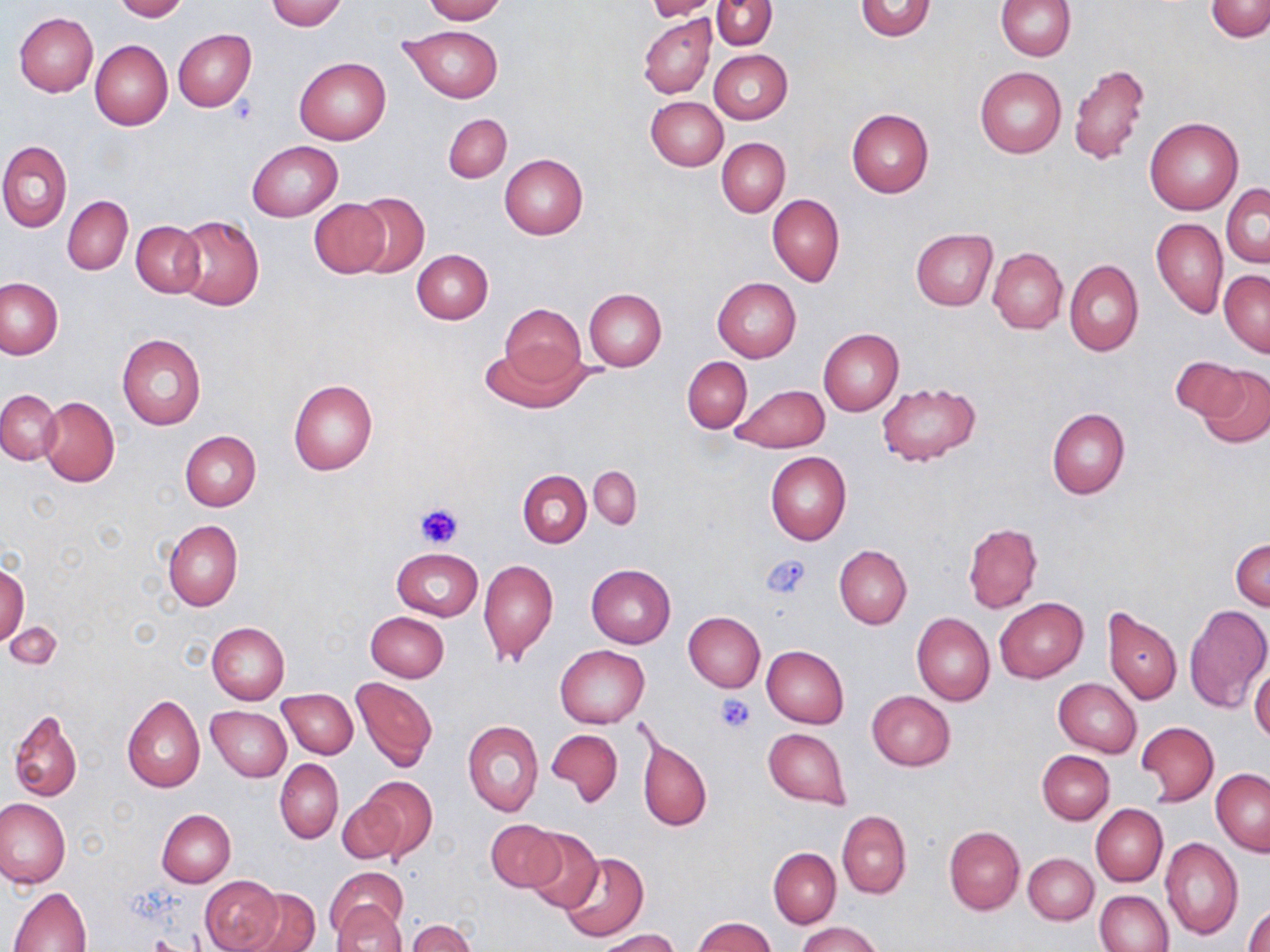

Approximate bounding boxes as (x1, y1, x2, y2) in pixels. Platelet locations: (227, 98, 258, 125), (416, 503, 464, 548), (764, 554, 812, 600), (715, 695, 755, 733). Uninfected red blood cell locations: (112, 0, 188, 21), (265, 0, 347, 31), (421, 0, 506, 23), (644, 0, 722, 20), (712, 0, 777, 50), (856, 0, 936, 40), (996, 0, 1076, 60), (1207, 1, 1270, 40), (13, 12, 98, 97), (639, 14, 715, 98), (398, 23, 503, 102), (173, 28, 256, 111), (90, 40, 172, 130), (710, 50, 791, 124), (294, 57, 392, 144), (1069, 64, 1150, 167), (974, 67, 1066, 158), (647, 96, 728, 170), (846, 110, 934, 198), (443, 113, 511, 183), (1145, 116, 1244, 215), (718, 138, 790, 217), (0, 140, 71, 232), (247, 140, 343, 222), (500, 153, 588, 239), (1222, 183, 1270, 267), (352, 192, 430, 278), (767, 194, 844, 286), (63, 196, 132, 274), (311, 200, 389, 277), (174, 215, 264, 311), (1151, 218, 1228, 320), (132, 220, 206, 297), (911, 228, 997, 310), (988, 247, 1067, 334), (412, 249, 493, 324), (1065, 259, 1143, 357), (1219, 269, 1270, 357), (713, 277, 801, 362), (0, 278, 61, 357), (583, 288, 667, 371), (499, 305, 586, 385), (819, 329, 903, 416), (117, 334, 206, 431), (483, 344, 585, 414), (682, 356, 752, 433), (1169, 356, 1250, 424), (1195, 365, 1270, 448), (288, 379, 378, 475), (877, 382, 982, 465), (729, 385, 828, 453), (0, 389, 61, 466), (39, 397, 120, 487), (1046, 406, 1130, 499), (179, 431, 260, 510), (765, 452, 851, 544), (590, 464, 639, 528), (518, 470, 591, 547), (162, 519, 243, 611), (963, 523, 1043, 613), (1232, 539, 1270, 611), (834, 544, 912, 628), (392, 548, 483, 621), (478, 558, 558, 663), (586, 564, 676, 647), (0, 565, 28, 645), (995, 597, 1089, 683), (1103, 605, 1181, 705), (1184, 605, 1270, 713), (366, 611, 448, 682), (683, 612, 765, 693), (912, 614, 995, 706), (6, 621, 63, 672), (207, 622, 289, 703), (555, 645, 649, 728), (761, 645, 848, 729), (1250, 668, 1270, 742), (351, 677, 437, 771), (1054, 678, 1140, 757), (278, 689, 358, 758), (865, 691, 955, 771), (122, 694, 205, 792), (207, 705, 291, 781), (7, 710, 81, 801), (463, 719, 543, 817), (1138, 721, 1218, 806), (762, 727, 850, 808), (546, 728, 623, 806), (636, 734, 712, 832), (1037, 750, 1114, 824), (275, 758, 343, 843), (1212, 769, 1270, 856), (357, 777, 437, 859), (337, 797, 407, 864), (0, 798, 70, 888), (1091, 804, 1168, 886), (156, 808, 235, 887), (837, 811, 911, 898), (486, 819, 566, 892), (943, 826, 1024, 913), (523, 828, 603, 914), (1160, 838, 1243, 940), (768, 847, 842, 928), (559, 852, 648, 942), (1024, 852, 1097, 924), (327, 867, 408, 938), (200, 875, 284, 952), (10, 887, 92, 952), (240, 888, 321, 952), (1094, 890, 1173, 952), (333, 901, 407, 952), (1246, 904, 1270, 952), (692, 917, 776, 952), (408, 919, 476, 952), (798, 921, 881, 952), (598, 929, 678, 952). Slide-level diagnosis: no evidence of blood parasites. Image is 1270×952 pixels. May-Grünwald-Giemsa stain. One field of a larger specimen. Thin blood film. Captured at 1000x magnification. Optical microscopy.